Point out each Plasmodium parasite.
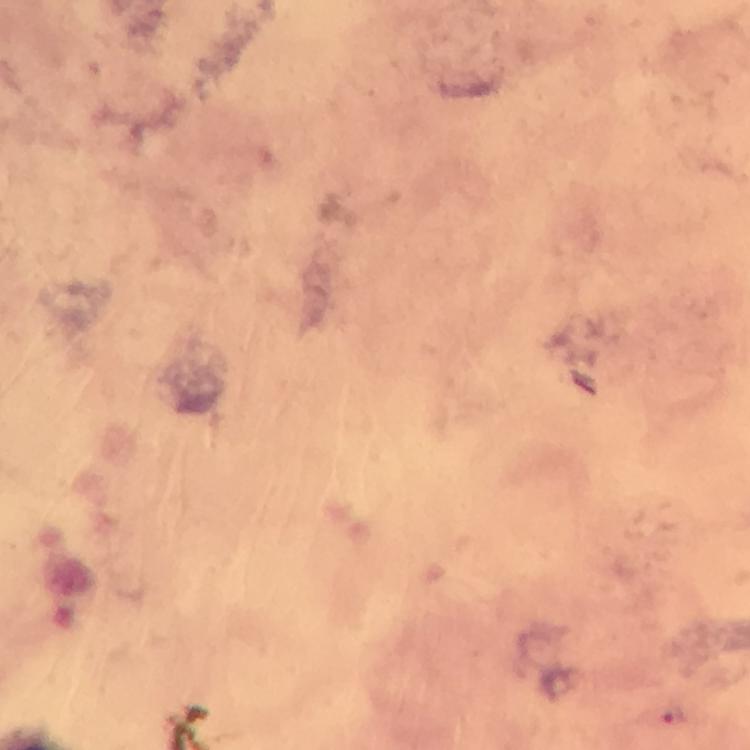
Approximate centers as (x, y) in pixels.
Plasmodium parasites: (675, 716).

stain: Giemsa
cropped_from: one field of view
preparation: thick blood smear
context: from a malaria diagnostic workup
magnification: 100x
immersion_oil: applied
capture: smartphone mounted on the microscope
image_size: 750×750 pixels